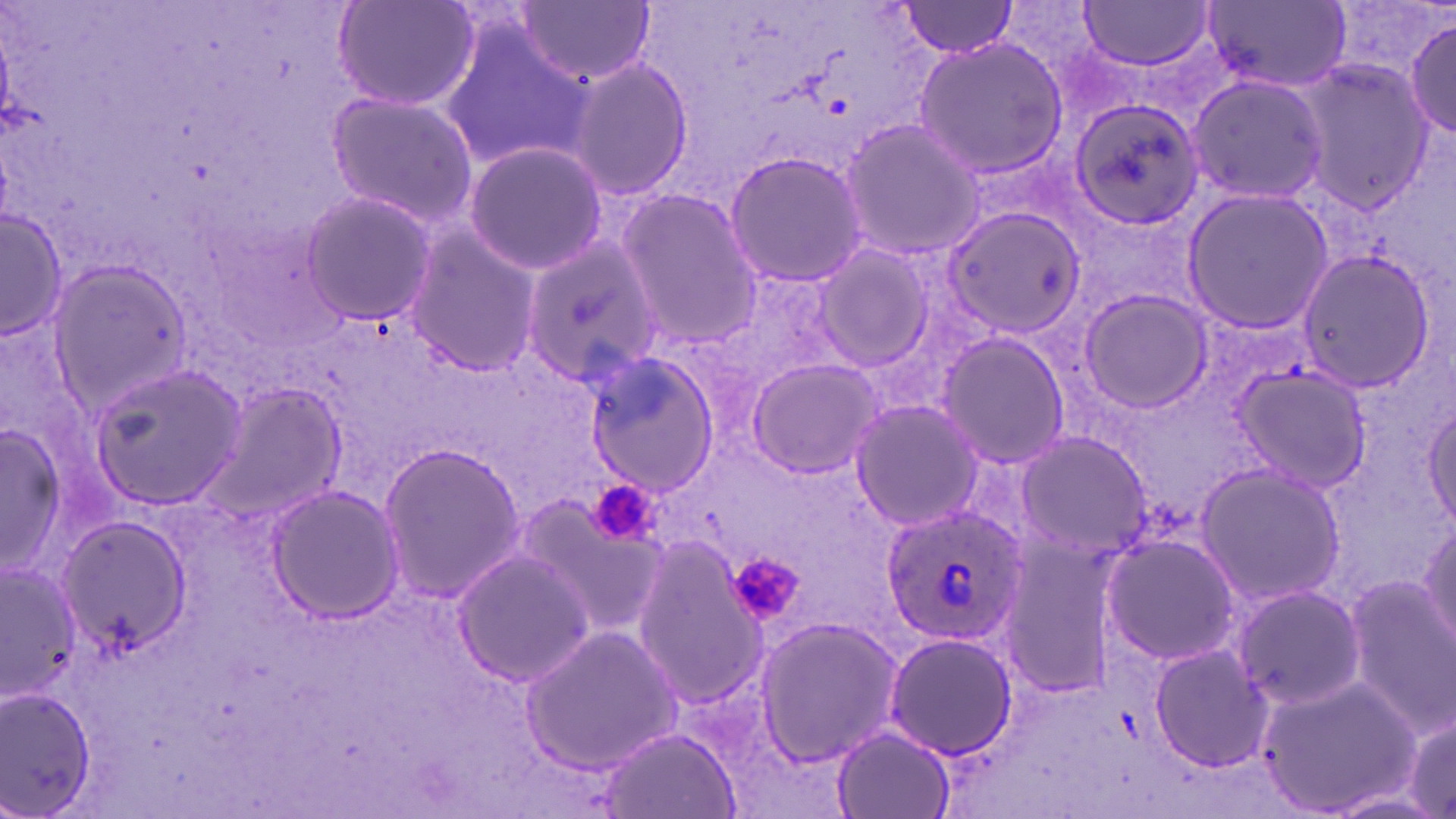
Approximate bounding boxes as (x1,y1)-(x2,y2) corner pairs in pixels. Uninfected red blood cell locations: (334,0)-(480,113), (518,1)-(655,86), (1202,1)-(1352,93), (897,2)-(1023,56), (1076,2)-(1218,71), (1405,18)-(1456,139), (440,20)-(593,169), (913,36)-(1070,179), (567,54)-(692,205), (1290,57)-(1436,216), (1186,72)-(1329,205), (322,89)-(480,227), (1066,97)-(1207,231), (839,118)-(983,260), (461,140)-(607,275), (724,149)-(869,287), (1178,186)-(1334,334), (619,187)-(763,349), (298,191)-(439,325), (941,205)-(1085,338), (1,208)-(66,342), (404,227)-(539,377), (524,239)-(661,381), (810,242)-(939,371), (1294,247)-(1438,395), (48,255)-(193,408), (1077,288)-(1212,416), (934,330)-(1071,470), (583,349)-(720,497), (745,356)-(884,479), (87,361)-(249,511), (1230,362)-(1368,494), (199,382)-(348,530), (850,399)-(986,532), (1423,399)-(1456,531), (0,418)-(72,582), (1012,429)-(1151,563), (376,440)-(526,603), (1194,461)-(1346,609), (265,484)-(408,624), (511,487)-(667,638), (57,513)-(191,654), (1417,516)-(1455,658), (1101,532)-(1244,666), (994,535)-(1123,697), (630,539)-(771,703), (451,547)-(595,688), (1,561)-(83,699), (1345,572)-(1455,735), (1227,582)-(1364,711), (753,616)-(904,769), (521,623)-(681,775), (884,631)-(1020,760), (1147,640)-(1276,776), (1260,672)-(1418,819), (0,684)-(101,819), (1393,700)-(1456,819), (597,726)-(741,818), (831,726)-(955,819). Platelet locations: (593,484)-(662,540), (726,551)-(807,627). Plasmodium ovale-infected red blood cell locations: (882,506)-(1028,647). Slide-level diagnosis: Plasmodium ovale. May-Grünwald-Giemsa-stained preparation. Captured at 1000x magnification. Light microscopy. One field of a larger specimen. Thin blood smear. Image is 1456×819 pixels.